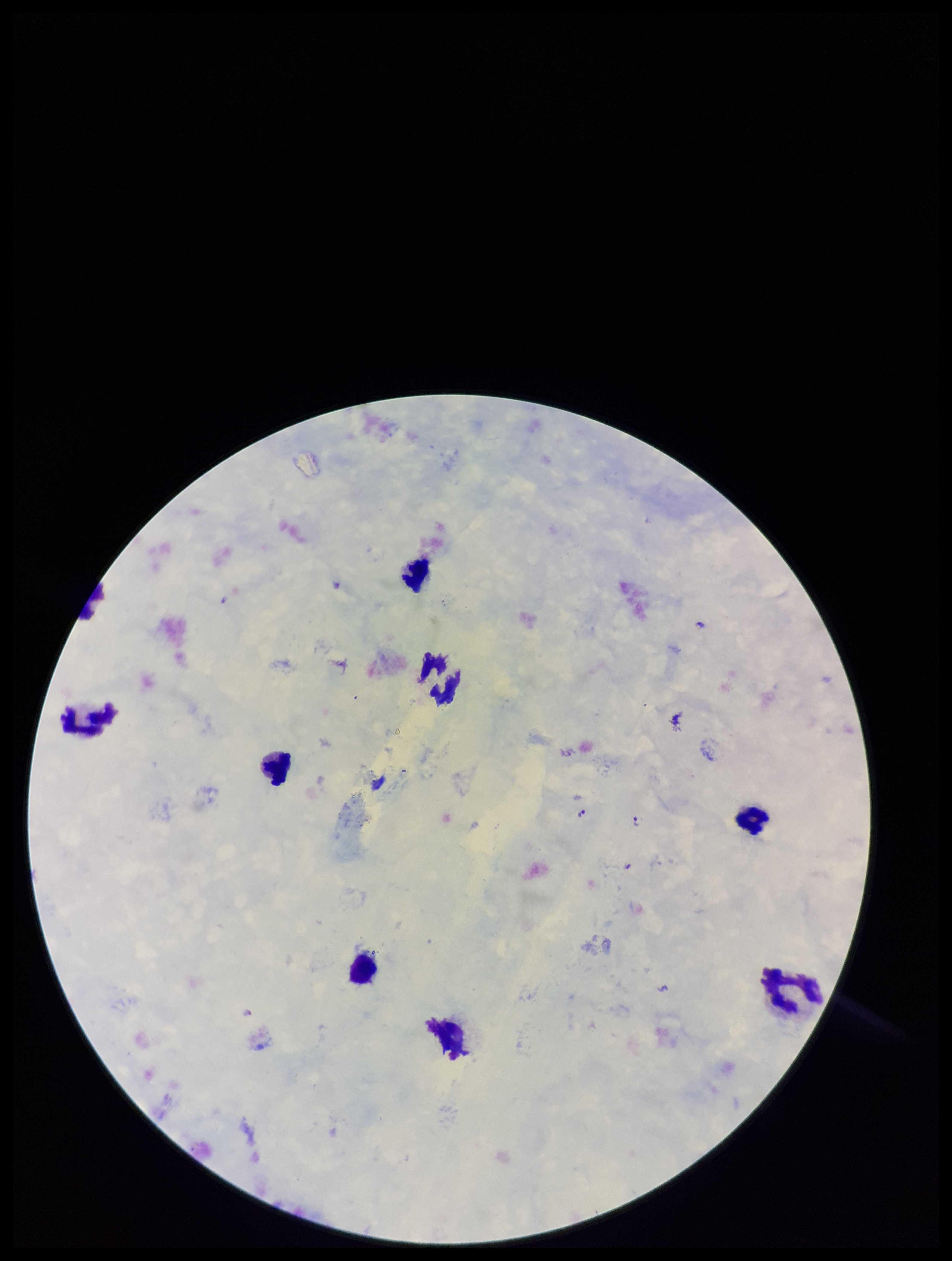

Summary:
  - Species reported for this patient: Plasmodium falciparum
  - Stain: Giemsa
  - Leukocyte count: 9
  - Parasite count: 2
  - Image size: 952×1261 pixels
  - Field of view: one from this slide
  - Patient malaria status: positive
  - Capture: smartphone photograph through the microscope eyepiece
  - Preparation: thick smear
  - Plasmodium parasites: detected